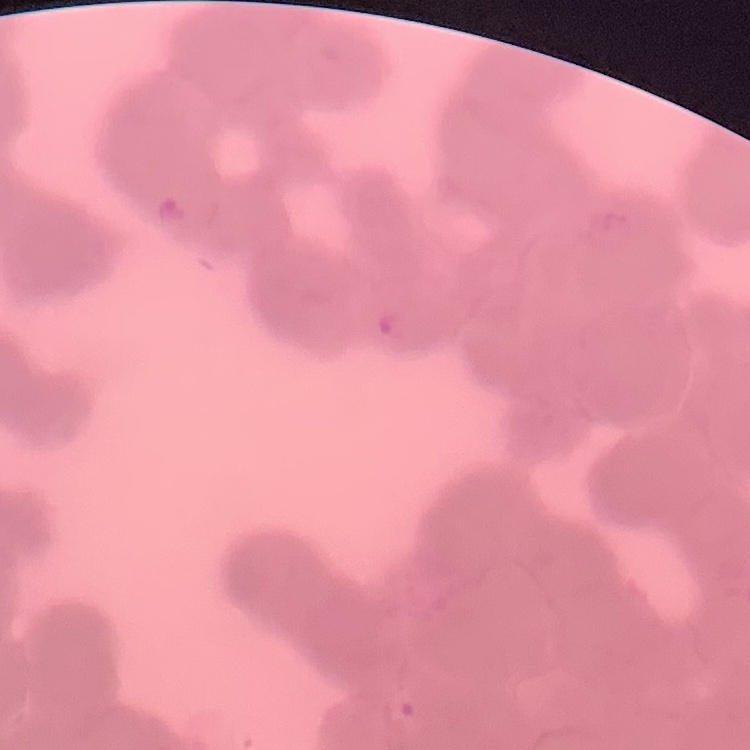
erythrocyte morphology = rouleaux formation
preparation = thin blood smear
stain = Field's or Giemsa
image type = square crop of a larger photomicrograph